Name the cell type shown.
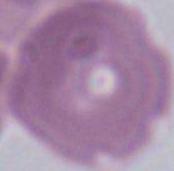

An erythrocyte.

Summary:
  - Magnification: 1000x
  - Modality: micrograph